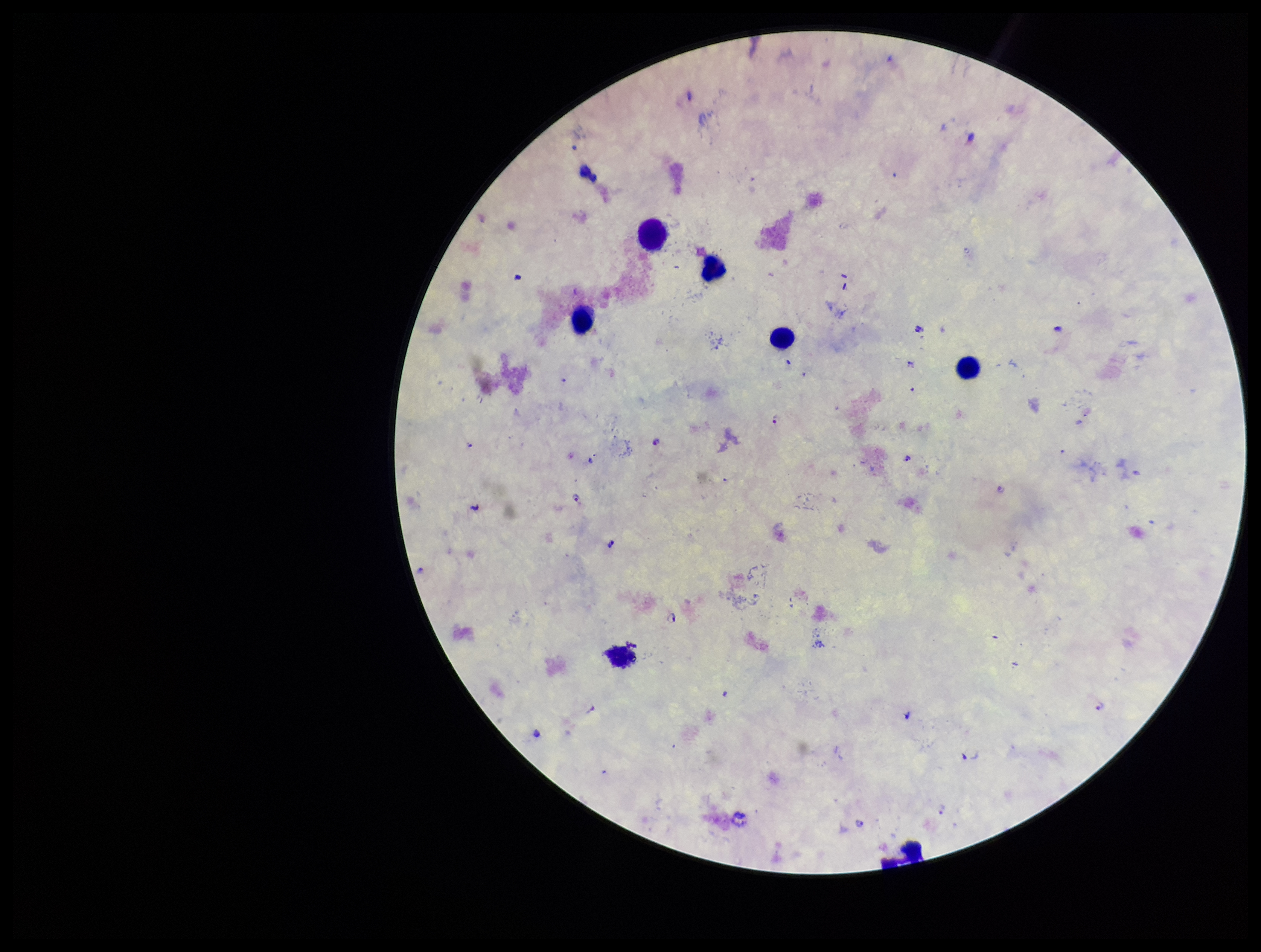

Summary:
  - Patient malaria status: positive
  - Image size: 1261×952 pixels
  - Stain: Giemsa
  - Leukocyte count: 7
  - Preparation: thick blood smear
  - Plasmodium parasites: detected
  - Capture: smartphone photograph through the microscope eyepiece
  - Parasite count: 13
  - Species reported for this patient: Plasmodium falciparum
  - Field of view: one from this slide